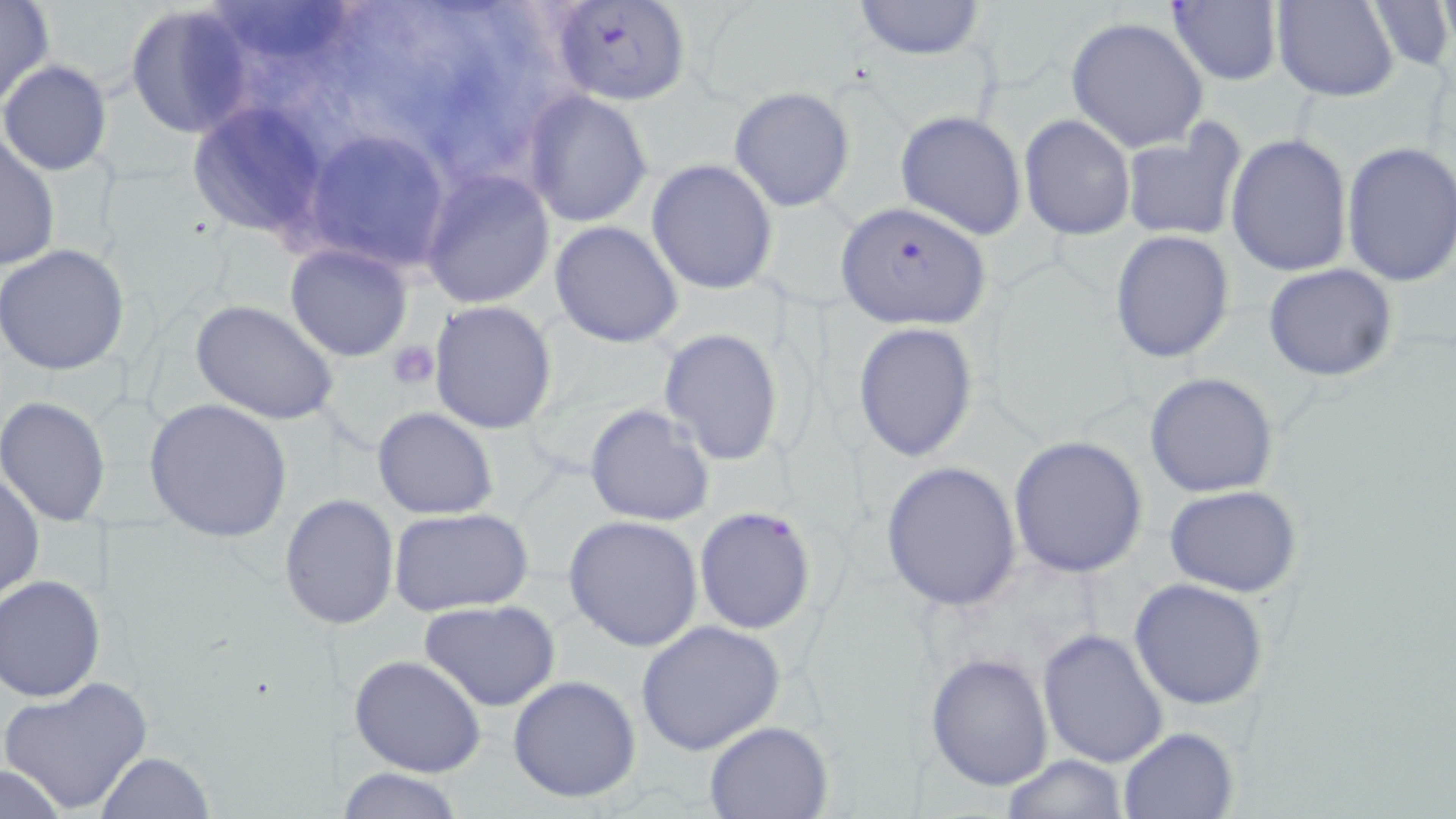 Approximate bounding boxes as [x1, y1, x2, y2] in pixels. Platelet locations: [390, 341, 440, 389]. Plasmodium falciparum-infected red blood cell locations: [549, 1, 690, 107], [834, 202, 992, 328]. Uninfected red blood cell locations: [0, 0, 55, 108], [218, 0, 357, 66], [1272, 0, 1399, 101], [1365, 0, 1454, 72], [850, 1, 986, 60], [124, 3, 254, 138], [1167, 3, 1283, 85], [1065, 15, 1208, 152], [1, 60, 111, 175], [729, 87, 853, 210], [524, 91, 652, 228], [186, 104, 333, 235], [895, 110, 1027, 239], [1019, 114, 1136, 240], [1120, 123, 1248, 243], [0, 130, 60, 273], [1225, 133, 1353, 276], [312, 141, 444, 261], [1339, 142, 1456, 290], [647, 159, 779, 295], [419, 169, 556, 309], [549, 221, 683, 349], [1110, 230, 1235, 362], [284, 242, 413, 361], [1, 243, 130, 377], [1263, 264, 1398, 382], [429, 299, 560, 435], [191, 301, 339, 425], [853, 322, 977, 461], [658, 327, 785, 467], [1144, 371, 1280, 498], [0, 396, 113, 526], [146, 398, 294, 542], [583, 404, 716, 528], [371, 407, 498, 521], [1007, 436, 1150, 578], [880, 462, 1024, 610], [1, 467, 45, 605], [1165, 485, 1303, 597], [279, 494, 400, 629], [693, 505, 817, 634], [388, 508, 533, 616], [563, 514, 705, 652], [0, 576, 106, 700], [1129, 578, 1269, 710], [420, 600, 563, 712], [636, 620, 788, 757], [1038, 626, 1169, 766], [925, 652, 1053, 792], [349, 654, 488, 777], [1, 674, 156, 816], [507, 675, 641, 804], [704, 720, 835, 819], [1118, 727, 1238, 818], [98, 751, 214, 818], [999, 753, 1130, 818], [0, 765, 73, 816], [336, 767, 467, 819]. Slide-level diagnosis: Plasmodium falciparum. Image is 1456×819 pixels. May-Grünwald-Giemsa stain. Optical microscopy. 1000x magnification. Single field of view. Thin blood smear.